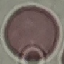

Result: no malaria parasites detected. Giemsa-stained preparation. Cell patch, automatically extracted from a larger field of view and resized to 64 × 64 pixels. Acquired by smartphone through the microscope eyepiece. Thin smear of blood.